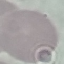
Summary:
  - Malaria status: uninfected
  - Image type: automatically extracted cell patch, resized to 64 × 64 pixels
  - Preparation: thin smear
  - Stain: Giemsa
  - Capture: smartphone through the microscope eyepiece